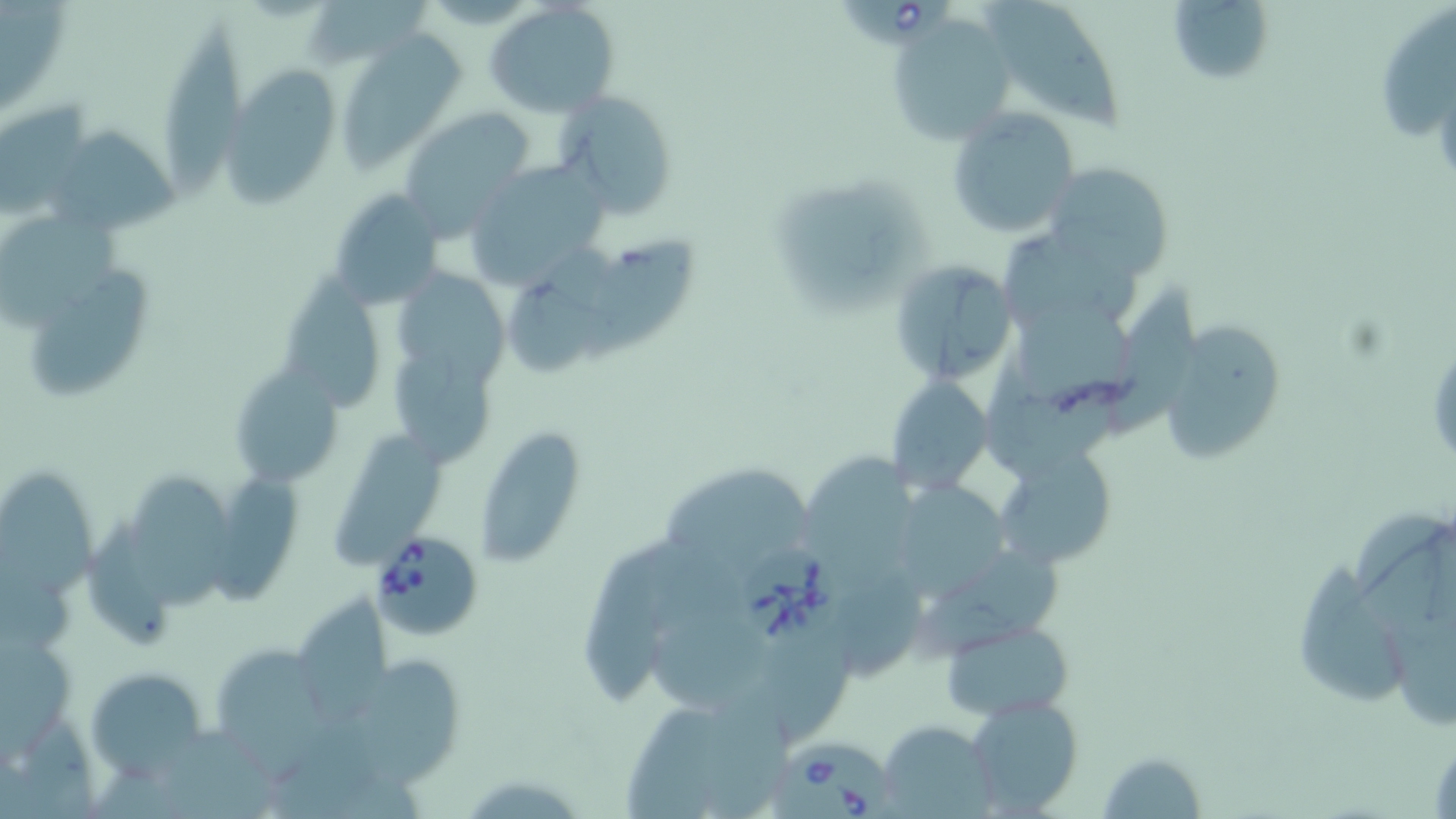

slide-level diagnosis = Babesia divergens
magnification = 1000x
field of view = one of a larger specimen
image size = 1456×819 pixels
Babesia divergens-infected red blood cell locations = approximate bounding boxes as (x1,y1)-(x2,y2) corner pairs in pixels: (834,0)-(953,43), (369,531)-(480,640), (743,542)-(845,647), (777,740)-(894,819)
uninfected red blood cell locations = approximate bounding boxes as (x1,y1)-(x2,y2) corner pairs in pixels: (305,0)-(436,73), (978,0)-(1132,134), (1167,0)-(1278,80), (484,3)-(620,116), (1379,7)-(1455,145), (164,16)-(244,205), (889,16)-(1018,146), (337,29)-(464,170), (225,67)-(336,203), (553,88)-(681,219), (0,100)-(91,222), (402,100)-(535,242), (946,107)-(1079,238), (48,125)-(180,236), (470,156)-(605,293), (1044,163)-(1173,277), (773,177)-(929,309), (326,189)-(443,306), (0,205)-(133,335), (995,229)-(1141,336), (584,235)-(702,366), (506,251)-(619,380), (889,261)-(1018,386), (395,262)-(512,382), (29,267)-(158,397), (290,271)-(381,418), (1105,281)-(1207,436), (1006,311)-(1135,427), (1160,313)-(1288,465), (392,345)-(496,466), (981,356)-(1113,480), (228,362)-(342,492), (884,376)-(994,495), (476,430)-(585,571), (336,431)-(447,571), (996,444)-(1120,568), (806,452)-(917,583), (133,466)-(235,612), (668,466)-(811,581), (1,467)-(95,599), (215,475)-(315,601), (904,478)-(1006,602), (1353,510)-(1456,647), (86,519)-(170,650), (584,541)-(690,705), (911,548)-(1069,662), (1293,552)-(1405,708), (303,591)-(392,723), (652,594)-(771,715), (944,619)-(1074,721), (760,631)-(863,741), (0,634)-(75,774), (223,645)-(333,781), (362,659)-(458,792), (86,666)-(209,776), (700,689)-(798,819), (966,694)-(1083,815), (629,703)-(726,819), (876,722)-(996,818), (168,727)-(277,819), (1097,751)-(1207,819)
modality = light microscopy
stain = May-Grünwald-Giemsa
preparation = thin blood film